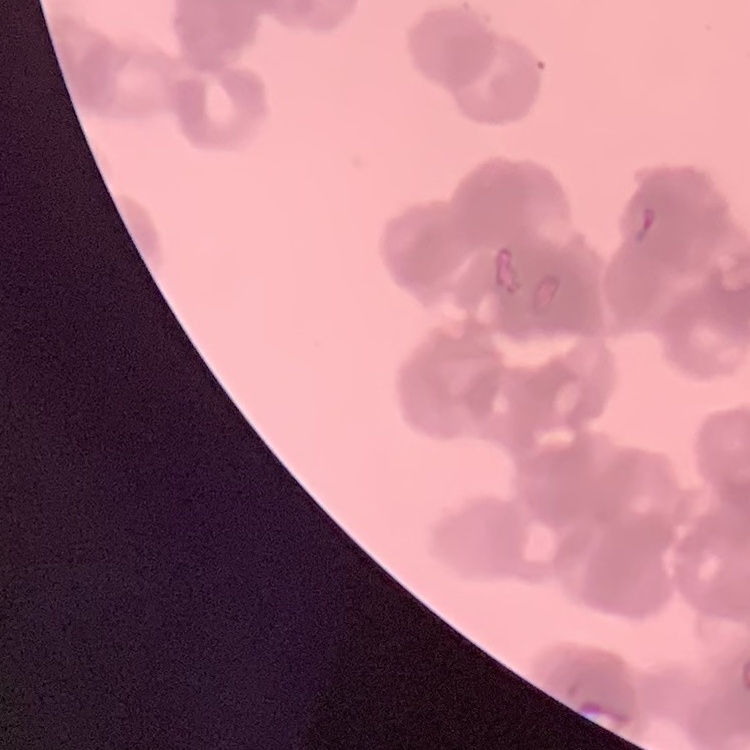
Summary:
  - Red blood cell morphology: rouleaux formation
  - Image type: square crop of a larger photomicrograph
  - Preparation: thin blood smear
  - Stain: Field's or Giemsa